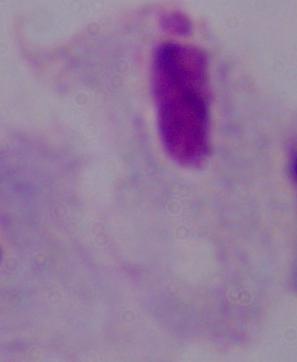 1000x magnification. A trichomonad is shown. Micrograph.